Comment on the morphology of the red blood cells.
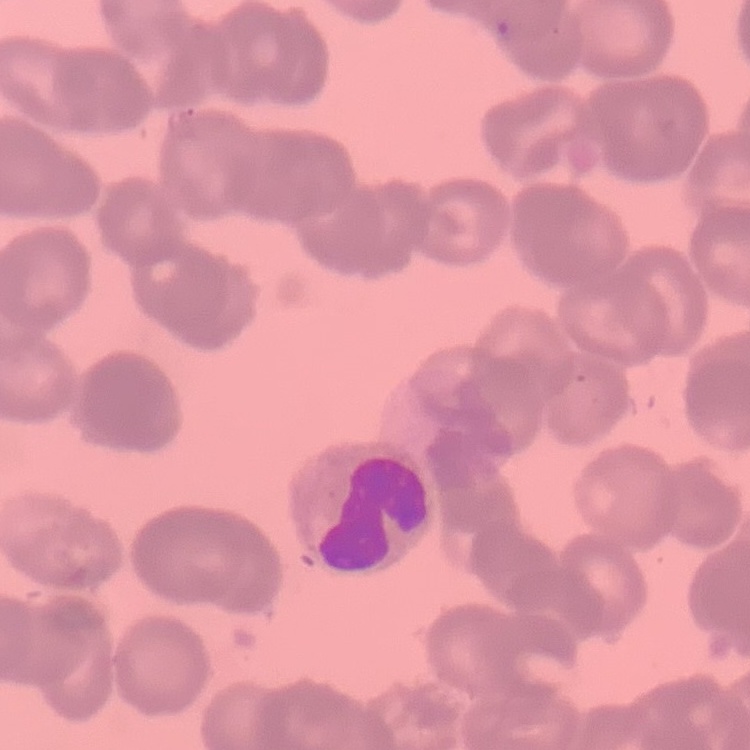

Rouleaux formation.

Summary:
  - Image type: square crop of a larger photomicrograph
  - Preparation: thin blood film
  - Stain: Field's or Giemsa